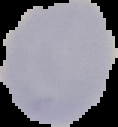 Malaria status: uninfected. Image is 118×127 pixels. From a thin blood film. The area outside the segmented cell region is set to black.